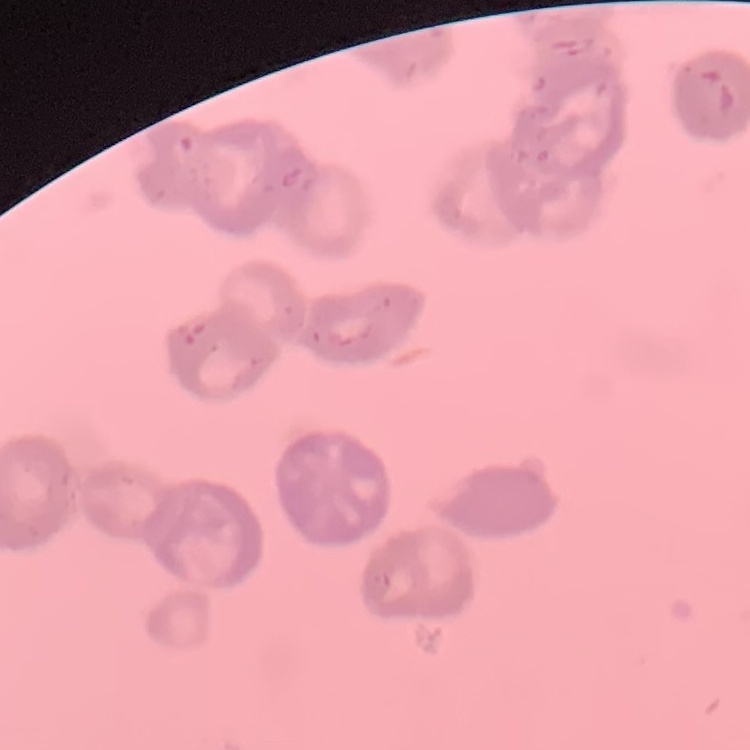

The red blood cells exhibit rouleaux formation. Thin peripheral smear. Field's or Giemsa stain. Square crop of a larger photomicrograph.